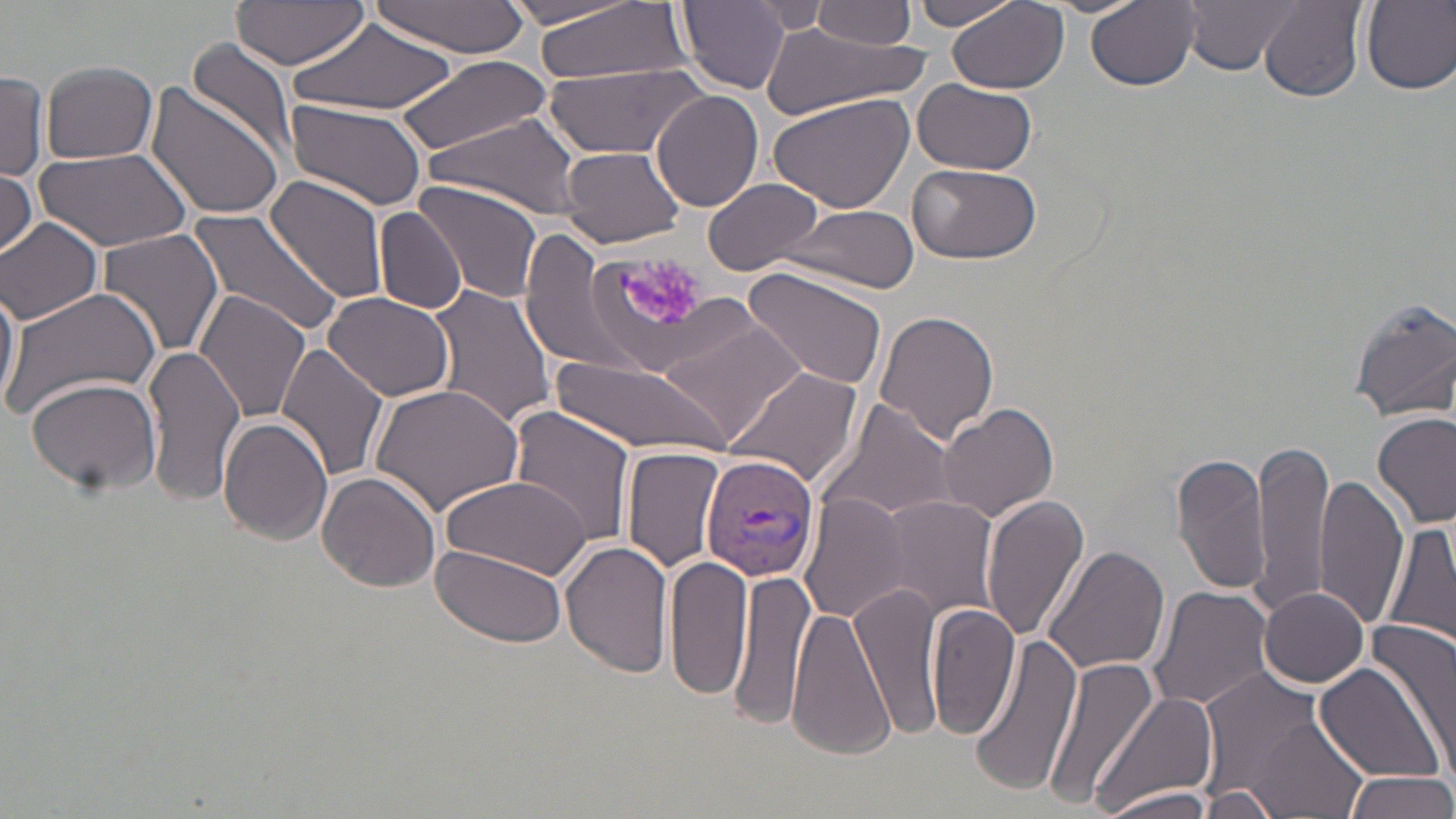

slide-level diagnosis = Plasmodium vivax
modality = optical microscopy
stain = May-Grünwald-Giemsa
image size = 1456×819 pixels
field of view = single
preparation = thin blood smear
magnification = 1000x
uninfected red blood cell locations = approximate bounding boxes as (x1, y1, x2, y2) in pixels: (372, 0, 528, 58), (530, 0, 689, 84), (1087, 0, 1202, 90), (1179, 0, 1307, 76), (232, 1, 370, 72), (906, 1, 1023, 31), (1258, 1, 1366, 102), (1359, 1, 1456, 94), (676, 2, 792, 94), (811, 2, 917, 50), (945, 2, 1072, 96), (748, 3, 831, 35), (287, 18, 457, 120), (761, 23, 924, 121), (189, 39, 300, 169), (396, 52, 552, 154), (542, 59, 706, 158), (40, 61, 158, 164), (0, 72, 48, 179), (914, 78, 1039, 175), (145, 83, 286, 223), (768, 89, 917, 214), (651, 90, 764, 211), (284, 99, 429, 212), (424, 117, 580, 216), (34, 146, 192, 254), (560, 146, 687, 248), (909, 162, 1040, 266), (0, 165, 39, 259), (264, 175, 391, 306), (412, 180, 546, 304), (701, 182, 825, 273), (782, 203, 919, 293), (354, 204, 464, 398), (375, 205, 468, 314), (185, 207, 346, 339), (0, 217, 103, 324), (95, 227, 222, 361), (520, 235, 635, 371), (584, 247, 724, 377), (742, 264, 888, 390), (0, 277, 19, 412), (427, 283, 557, 432), (1, 286, 162, 423), (195, 290, 312, 424), (322, 290, 457, 401), (1347, 297, 1456, 423), (874, 310, 1000, 446), (664, 315, 808, 445), (143, 344, 246, 505), (277, 344, 391, 486), (551, 361, 730, 456), (725, 368, 863, 489), (25, 377, 163, 493), (368, 381, 525, 516), (818, 400, 955, 523), (936, 401, 1059, 521), (510, 406, 636, 546), (1373, 411, 1455, 528), (218, 417, 333, 545), (1251, 437, 1334, 619), (622, 447, 727, 574), (1171, 451, 1270, 596), (315, 470, 442, 593), (1314, 471, 1409, 631), (439, 474, 592, 579), (981, 493, 1090, 644), (800, 495, 912, 624), (880, 496, 998, 620), (1382, 520, 1456, 652), (561, 537, 675, 680), (432, 544, 569, 647), (1041, 545, 1169, 677), (666, 554, 754, 700), (731, 570, 816, 729), (852, 582, 942, 740), (1147, 586, 1275, 716), (1259, 587, 1371, 689), (928, 602, 1021, 743), (788, 606, 894, 762), (1364, 624, 1456, 760), (974, 639, 1084, 797), (1046, 655, 1162, 813), (1315, 663, 1449, 784), (1195, 671, 1331, 793), (1093, 691, 1218, 819), (1248, 719, 1365, 818), (1340, 769, 1455, 819), (1093, 787, 1222, 819), (1198, 787, 1280, 818)
Plasmodium vivax-infected red blood cell locations = approximate bounding boxes as (x1, y1, x2, y2) in pixels: (701, 451, 822, 579)
platelet locations = approximate bounding boxes as (x1, y1, x2, y2) in pixels: (624, 257, 703, 327)